Point out each Plasmodium parasite.
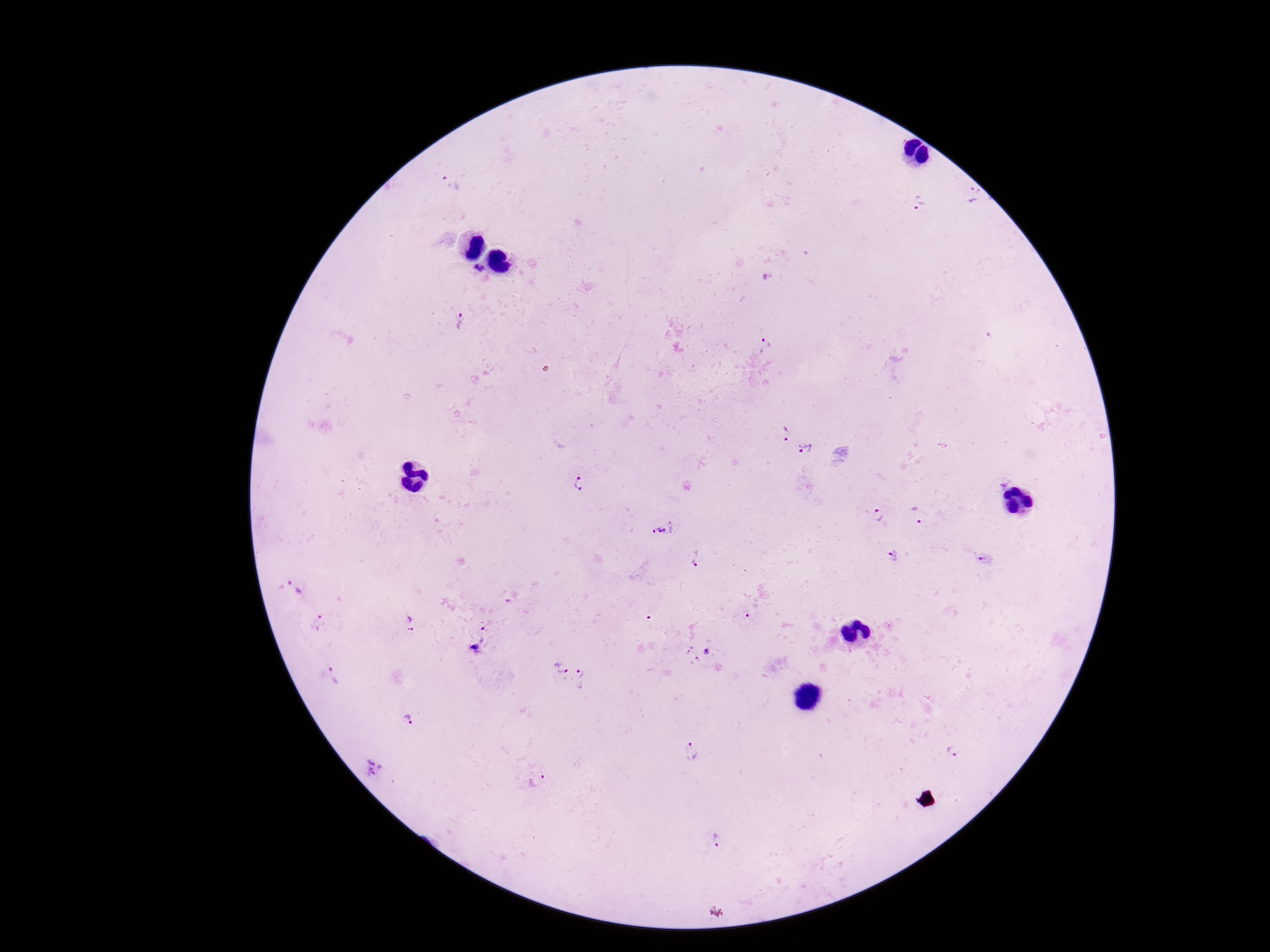

Approximate centers as {x, y} in pixels.
Plasmodium parasites: {450, 184}, {974, 195}, {920, 202}, {480, 270}, {460, 321}, {763, 346}, {785, 433}, {806, 450}, {580, 484}, {878, 516}, {920, 516}, {663, 527}, {894, 556}, {697, 558}, {984, 559}, {295, 589}, {751, 610}, {318, 624}, {410, 624}, {487, 625}, {477, 648}, {696, 652}, {560, 666}, {335, 675}, {585, 680}, {409, 720}, {690, 751}, {953, 751}, {376, 770}, {538, 780}, {716, 840}.

Summary:
  - Field of view: one from this slide
  - Image size: 1270×952 pixels
  - Magnification: 100x
  - Preparation: thick blood smear
  - Patient malaria status: positive
  - Capture: smartphone camera through the microscope eyepiece
  - Stain: Giemsa